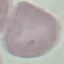
Summary:
  - Result: no malaria parasites detected
  - Image type: automatically extracted cell patch, resized to 64 × 64 pixels
  - Preparation: thin smear
  - Capture: smartphone through the microscope eyepiece
  - Stain: Giemsa